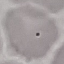
{
  "result": "no malaria parasites detected",
  "preparation": "thin blood smear",
  "image_type": "cell patch, automatically extracted from a larger field of view and resized to 64 × 64 pixels",
  "capture": "smartphone camera at the microscope eyepiece",
  "stain": "Giemsa"
}